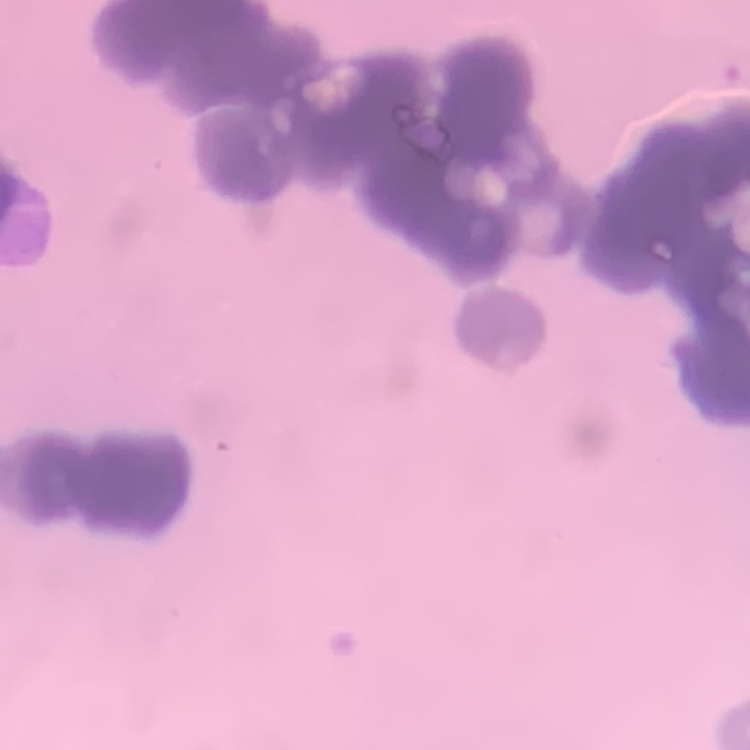

{
  "erythrocyte_morphology": "rouleaux formation",
  "preparation": "thin blood film",
  "stain": "Field's or Giemsa",
  "image_type": "square crop of a larger photomicrograph"
}